Report the malaria status of this cell.
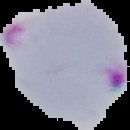
It is parasitized.

Cell region segmented out of the field of view; the surrounding area is masked to black. From a thin blood smear. Image is 130×130 pixels.